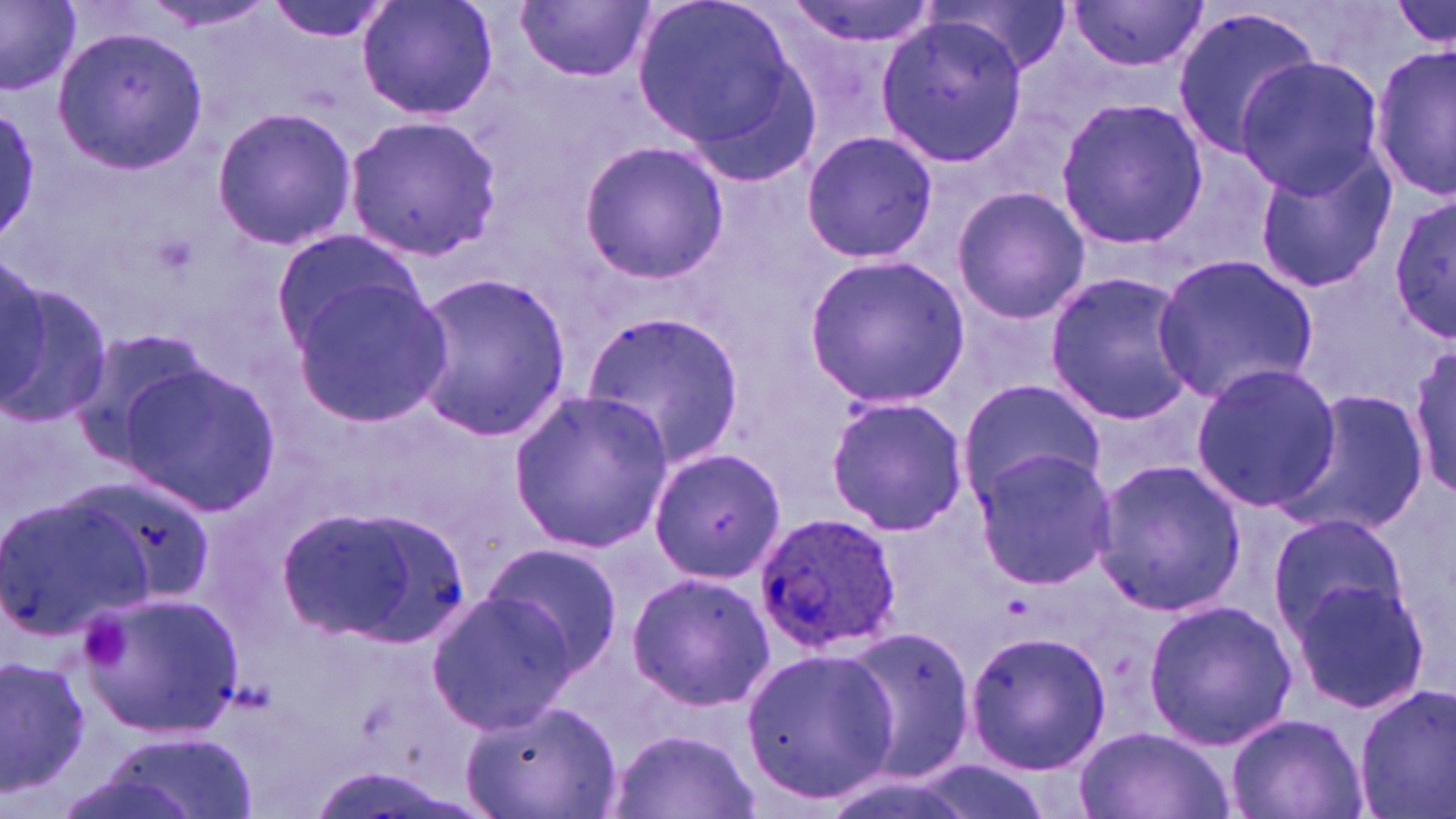

slide-level diagnosis = Plasmodium ovale
modality = light microscopy
Plasmodium ovale-infected red blood cell locations = approximate bounding boxes as (x1,y1)-(x2,y2) corner pairs in pixels: (755,511)-(904,655)
stain = May-Grünwald-Giemsa
preparation = thin blood smear
field of view = single
image size = 1456×819 pixels
magnification = 1000x
uninfected red blood cell locations = approximate bounding boxes as (x1,y1)-(x2,y2) corner pairs in pixels: (259,0)-(396,44), (357,0)-(498,123), (518,0)-(653,82), (632,0)-(820,171), (784,0)-(942,49), (0,1)-(79,95), (136,1)-(280,34), (1067,2)-(1209,72), (1170,9)-(1322,156), (873,11)-(1033,165), (53,27)-(206,174), (1371,46)-(1455,199), (1237,57)-(1385,196), (1054,95)-(1209,251), (0,101)-(43,251), (210,105)-(358,251), (343,115)-(501,259), (799,129)-(937,265), (578,138)-(729,286), (1248,145)-(1396,295), (950,186)-(1090,324), (1391,191)-(1454,345), (271,227)-(426,357), (1,251)-(50,413), (1152,254)-(1320,405), (805,255)-(970,405), (0,270)-(111,433), (1043,270)-(1199,428), (405,271)-(573,441), (285,277)-(452,427), (579,310)-(748,466), (66,324)-(220,469), (1408,340)-(1456,498), (118,361)-(281,517), (1188,361)-(1342,514), (956,381)-(1104,499), (1278,385)-(1431,537), (509,390)-(673,551), (825,394)-(968,536), (647,449)-(784,584), (970,449)-(1117,587), (1090,458)-(1247,618), (0,485)-(159,644), (280,501)-(464,650), (1266,511)-(1410,639), (481,541)-(624,677), (625,570)-(773,711), (1287,575)-(1431,714), (85,587)-(244,736), (426,587)-(575,735), (1142,599)-(1297,751), (831,626)-(977,783), (963,629)-(1110,774), (740,647)-(898,803), (0,654)-(93,797), (1352,684)-(1456,819), (462,698)-(618,818), (1227,712)-(1366,819), (1078,726)-(1233,819), (609,730)-(755,819)